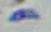

Summary:
  - Identification: Toxoplasma gondii
  - Magnification: 1000x
  - Modality: micrograph